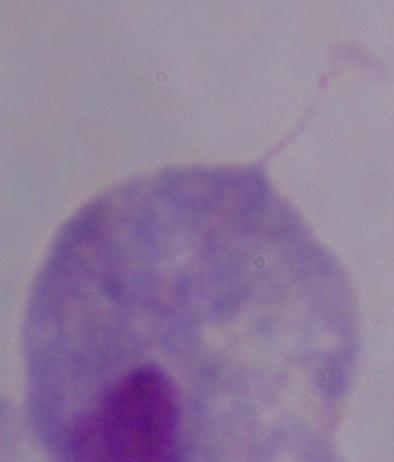
Summary:
  - Modality: photomicrograph
  - Identification: trichomonad
  - Magnification: 1000x